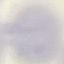

Summary:
  - Malaria status: uninfected
  - Capture: smartphone through the microscope eyepiece
  - Image type: cell patch, automatically extracted from a larger field of view and resized to 64 × 64 pixels
  - Preparation: thin blood film
  - Stain: Giemsa